Comment on the morphology of the erythrocytes.
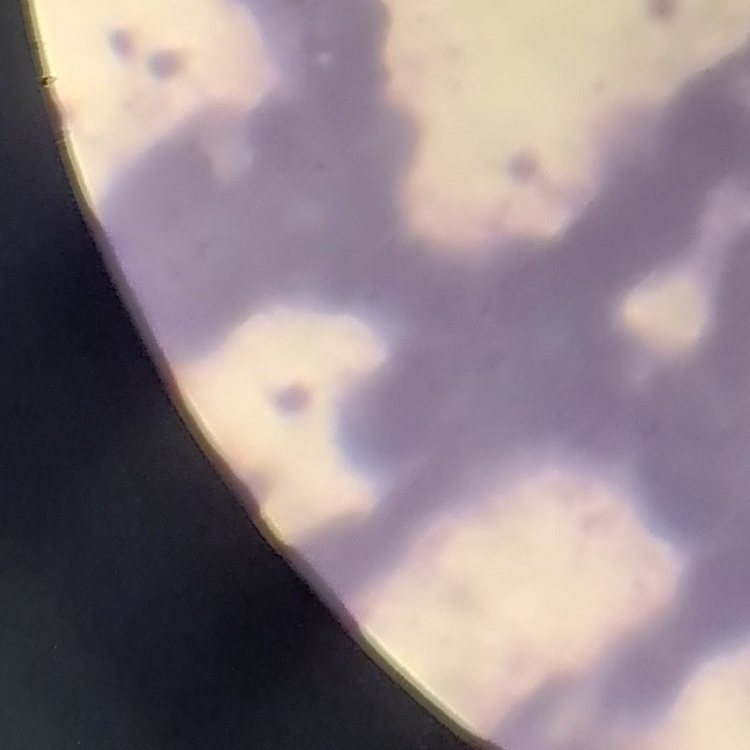
Rouleaux formation.

Thin blood film. One tile cut from a larger photomicrograph. Stained with either Field's or Giemsa.